Assess this cell for malaria.
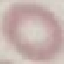
Uninfected.

Automatically extracted cell patch, resized to 64 × 64 pixels. Thin smear of blood. Photographed with a smartphone camera at the microscope eyepiece. Giemsa-stained preparation.